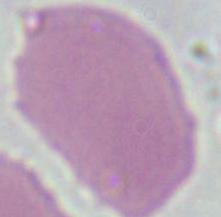
{
  "identification": "erythrocyte",
  "modality": "micrograph",
  "magnification": "1000x"
}